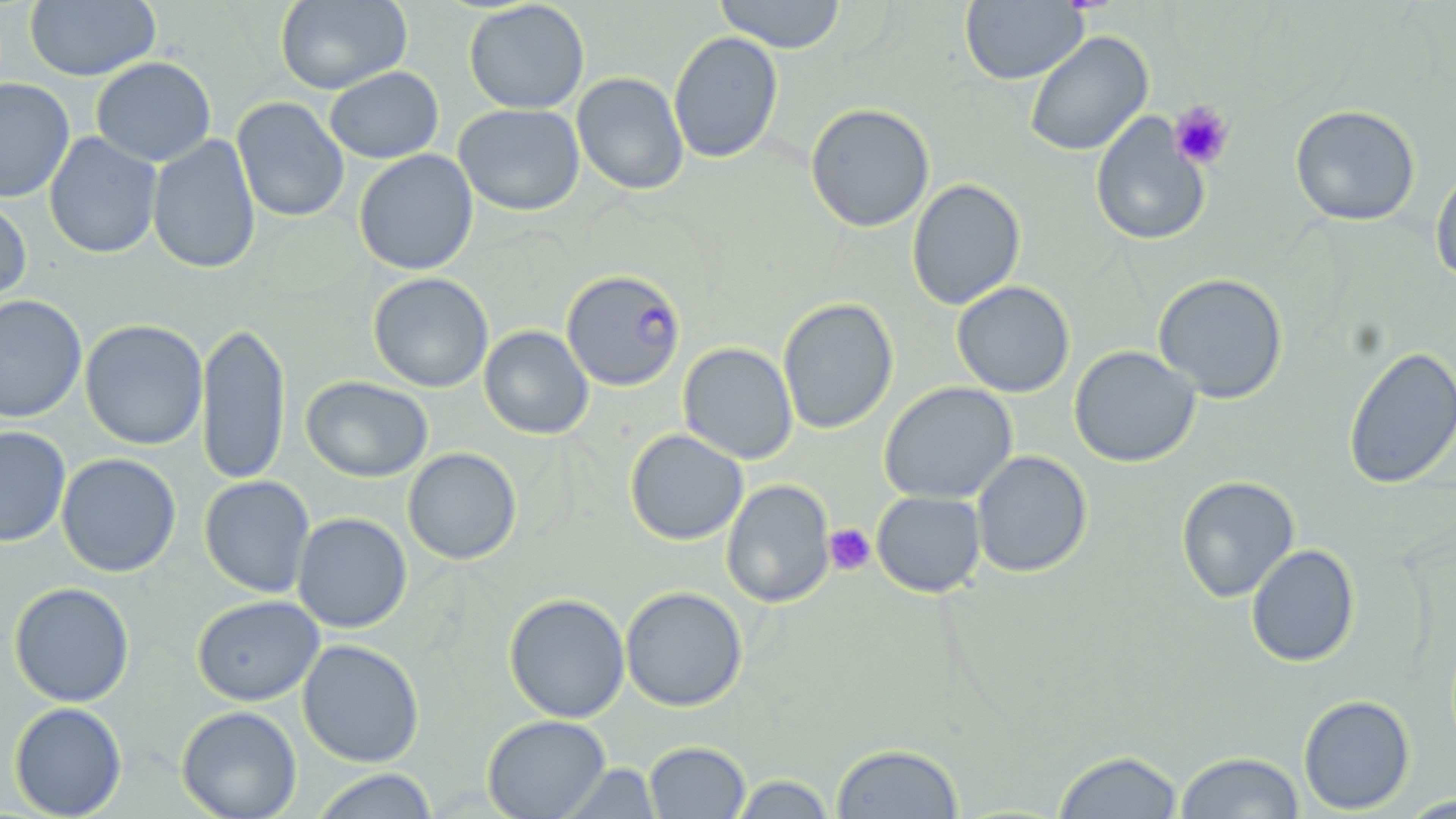
slide-level diagnosis = Plasmodium falciparum
field of view = single
uninfected red blood cell locations = approximate bounding boxes as (x1,y1)-(x2,y2) corner pairs in pixels: (25,0)-(160,81), (274,0)-(412,94), (713,0)-(847,53), (463,1)-(590,114), (960,1)-(1087,85), (668,31)-(784,164), (1024,31)-(1153,157), (90,56)-(216,166), (323,66)-(444,164), (572,72)-(689,195), (0,78)-(75,203), (231,96)-(350,223), (453,103)-(585,216), (805,103)-(934,232), (1289,104)-(1421,226), (1090,112)-(1210,247), (44,131)-(162,259), (147,134)-(261,275), (354,149)-(478,276), (1430,162)-(1456,286), (907,178)-(1026,310), (0,195)-(32,307), (367,272)-(494,393), (1152,273)-(1289,403), (952,281)-(1075,397), (0,294)-(87,423), (777,298)-(898,434), (79,319)-(209,450), (197,320)-(290,488), (479,325)-(594,439), (678,342)-(798,464), (1342,345)-(1456,490), (1069,346)-(1201,467), (300,376)-(433,482), (879,382)-(1018,504), (0,426)-(71,547), (625,429)-(748,545), (402,447)-(521,565), (971,450)-(1092,578), (56,453)-(181,577), (199,475)-(315,598), (1176,475)-(1299,603), (721,479)-(835,608), (872,491)-(986,597), (292,512)-(412,633), (1246,544)-(1360,667), (9,582)-(135,706), (620,586)-(747,712), (504,593)-(630,722), (191,594)-(324,705), (297,639)-(425,767), (1298,694)-(1415,815), (9,702)-(127,818), (176,705)-(302,819), (482,714)-(611,819), (643,741)-(751,818), (830,743)-(964,818), (1052,749)-(1184,818), (1174,751)-(1305,818), (558,762)-(663,818), (309,769)-(439,819), (729,773)-(837,818), (1396,794)-(1455,818)
Plasmodium falciparum-infected red blood cell locations = approximate bounding boxes as (x1,y1)-(x2,y2) corner pairs in pixels: (562,269)-(686,392)
image size = 1456×819 pixels
modality = optical microscopy
magnification = 1000x
platelet locations = approximate bounding boxes as (x1,y1)-(x2,y2) corner pairs in pixels: (1169,100)-(1235,170), (824,524)-(875,575)
preparation = thin blood smear
stain = May-Grünwald-Giemsa